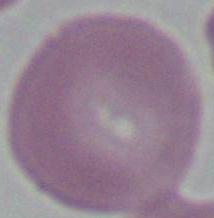

1000x magnification. Photomicrograph. A red blood cell is seen.